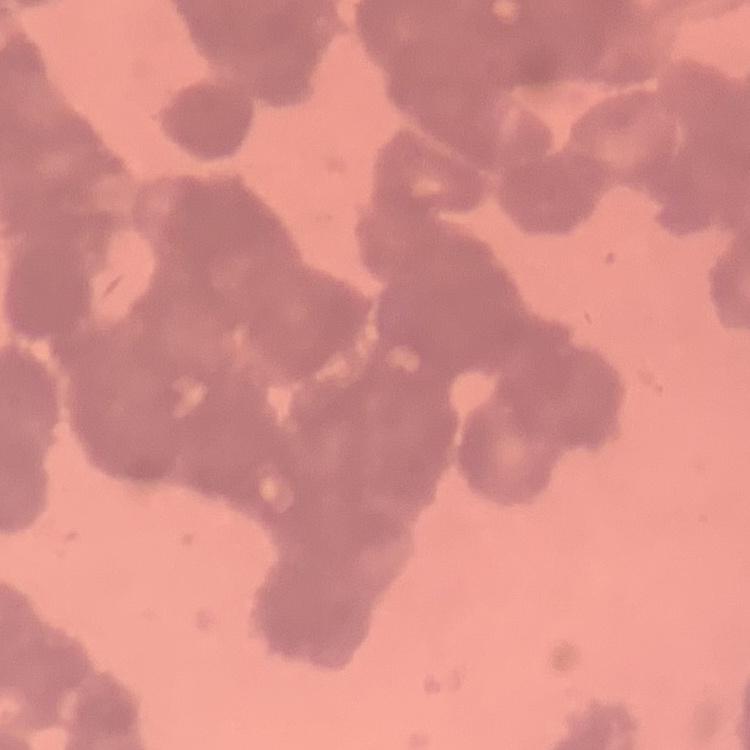
Summary:
  - Erythrocyte morphology: rouleaux formation
  - Preparation: thin blood film
  - Stain: Field's or Giemsa
  - Image type: square crop of a larger photomicrograph